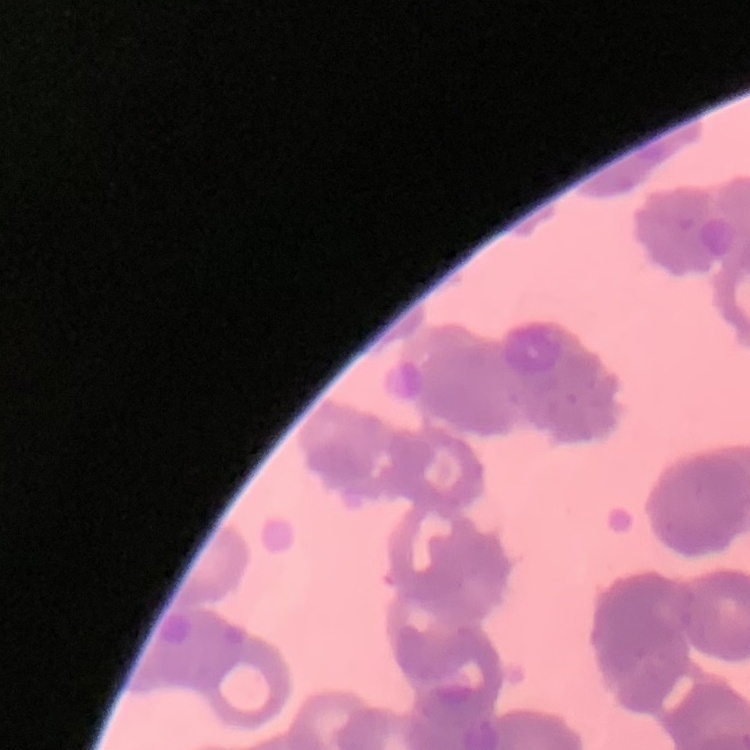 The red blood cells exhibit rouleaux formation. Field's or Giemsa stain. Square crop of a larger photomicrograph. Thin peripheral smear.